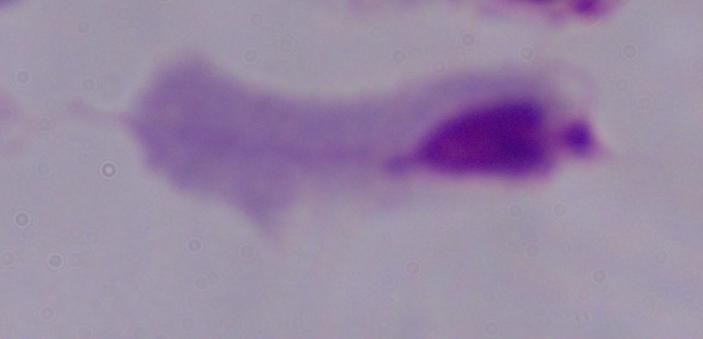
{
  "magnification": "1000x",
  "modality": "photomicrograph",
  "identification": "trichomonad"
}